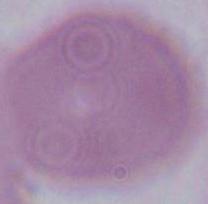
{
  "modality": "micrograph",
  "magnification": "1000x",
  "identification": "erythrocyte"
}